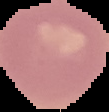

{
  "malaria_status": "uninfected",
  "image_size": "109×112 pixels",
  "preparation": "thin blood smear",
  "image_type": "cell region segmented out of the field of view; surrounding area masked to black"
}